Classify this cell by malaria status.
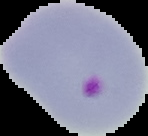

Parasitized.

preparation: thin blood smear
image_type: cell region segmented out of the field of view; surrounding area masked to black
image_size: 148×136 pixels